Give the preparation type.
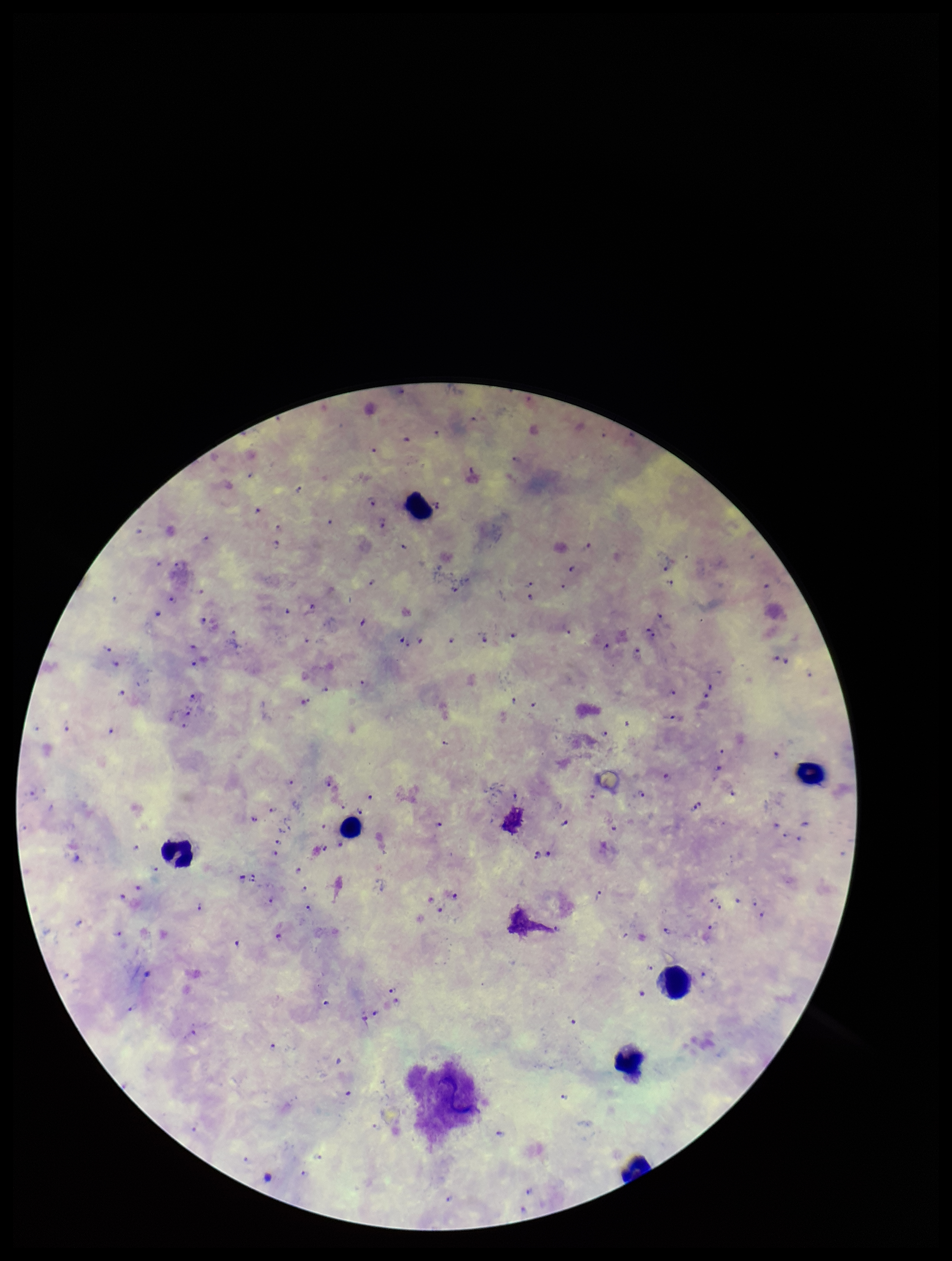
A thick smear.

species reported for this patient = Plasmodium falciparum
patient malaria status = infected
capture = smartphone photograph through the microscope eyepiece
image size = 952×1261 pixels
parasite count = 120
stain = Giemsa
Plasmodium parasites = detected
leukocyte count = 7
field of view = one from this slide